Assess this cell for malaria.
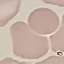

Uninfected.

Cell patch, automatically extracted from a larger field of view and resized to 64 × 64 pixels. Acquired by smartphone through the microscope eyepiece. Giemsa-stained preparation. Thin blood film.